Identify the blood parasite species.
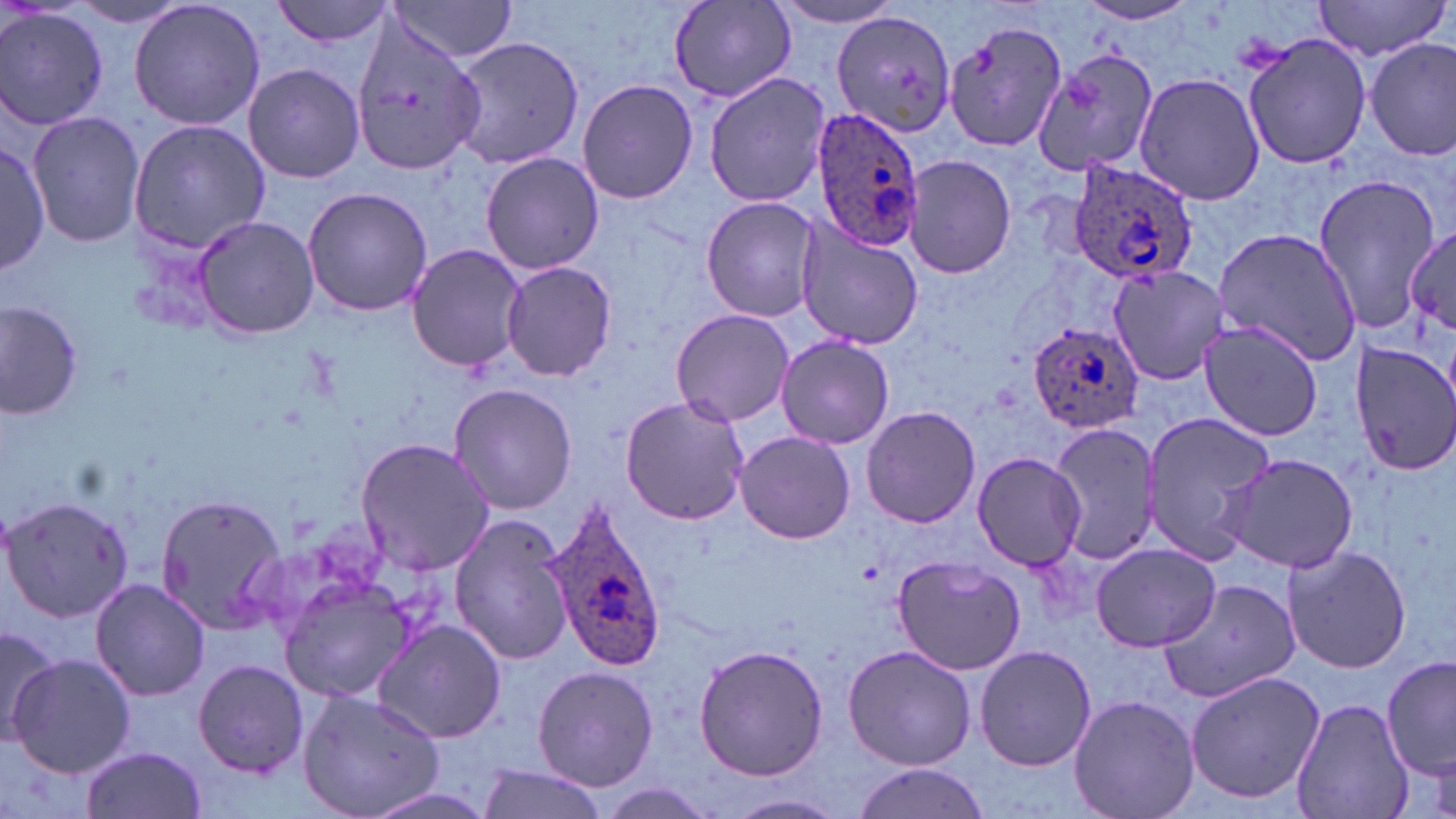

Plasmodium ovale.

preparation = thin blood smear
Plasmodium ovale-infected red blood cell locations = approximate bounding boxes as (x1,y1)-(x2,y2) corner pairs in pixels: (808,108)-(924,253), (1066,157)-(1199,286), (1027,324)-(1144,436), (540,498)-(667,675)
stain = May-Grünwald-Giemsa
image size = 1456×819 pixels
modality = optical microscopy
uninfected red blood cell locations = approximate bounding boxes as (x1,y1)-(x2,y2) corner pairs in pixels: (127,0)-(266,132), (269,0)-(399,48), (1078,0)-(1197,26), (1311,0)-(1449,62), (384,1)-(521,61), (667,1)-(796,103), (763,1)-(906,29), (1,7)-(110,133), (832,10)-(958,136), (350,14)-(489,175), (945,19)-(1066,153), (1242,32)-(1371,171), (444,34)-(587,172), (1365,35)-(1456,162), (1034,46)-(1161,177), (243,63)-(366,184), (703,71)-(833,207), (1135,72)-(1265,206), (576,79)-(698,204), (26,109)-(146,250), (127,119)-(271,252), (0,137)-(51,276), (481,151)-(603,276), (904,155)-(1018,279), (1310,169)-(1440,334), (303,188)-(434,318), (699,196)-(821,321), (192,216)-(320,340), (795,222)-(924,350), (1405,226)-(1456,332), (1210,228)-(1364,365), (407,241)-(525,375), (501,261)-(618,381), (1107,264)-(1233,385), (1,299)-(83,419), (670,309)-(795,427), (1198,320)-(1323,442), (775,335)-(895,450), (1350,340)-(1455,476), (448,383)-(578,514), (621,395)-(750,526), (860,407)-(982,528), (1139,411)-(1280,565), (1047,420)-(1163,568), (735,430)-(855,544), (354,437)-(494,574), (971,450)-(1088,570), (1219,453)-(1360,573), (152,490)-(292,633), (0,496)-(131,625), (451,513)-(575,664), (1090,542)-(1221,653), (1282,543)-(1413,674), (890,555)-(1026,675), (90,577)-(212,700), (1159,578)-(1300,702), (278,580)-(412,704), (373,618)-(508,743), (0,622)-(59,746), (693,644)-(829,780), (973,644)-(1096,772), (843,646)-(977,770), (1381,652)-(1454,784), (9,653)-(137,777), (193,659)-(308,777), (533,665)-(658,791), (1185,669)-(1326,806), (297,687)-(444,819), (1068,695)-(1201,819), (1291,697)-(1415,819), (79,745)-(208,819), (850,761)-(995,819), (475,763)-(609,819), (593,781)-(723,818), (353,785)-(504,819), (717,790)-(848,818)
magnification = 1000x
field of view = single